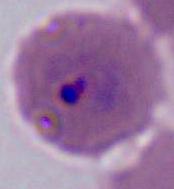
Captured at either 400x or 1000x magnification. Micrograph. A Plasmodium parasite is shown.